State which parasite is depicted.
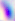

This is Toxoplasma gondii.

Summary:
  - Modality: micrograph
  - Magnification: 400x